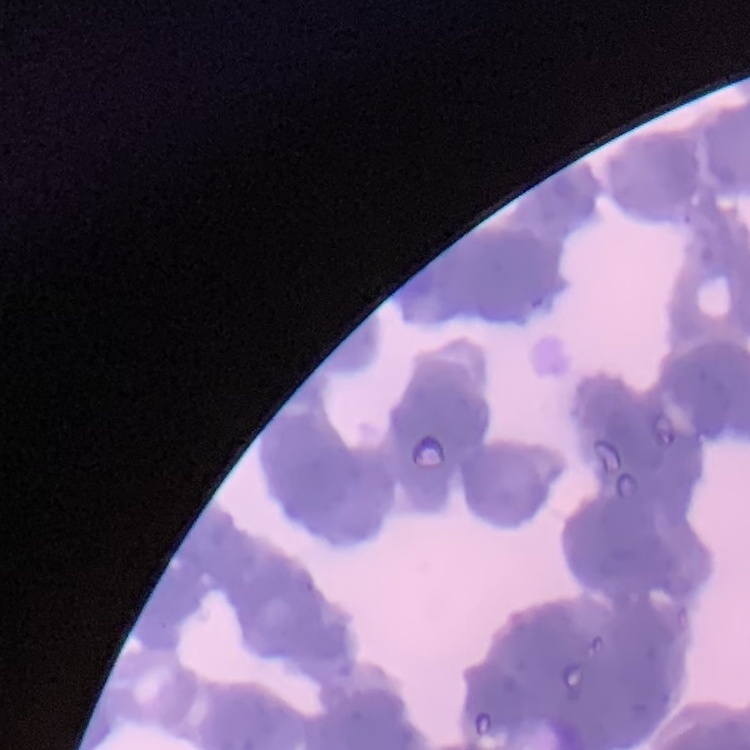
The red blood cells show rouleaux formation. Thin peripheral smear. Field's or Giemsa stain. One tile cut from a larger photomicrograph.